Assess this cell for malaria.
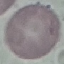
Uninfected.

preparation = thin blood smear
image type = automatically extracted cell patch, resized to 64 × 64 pixels
stain = Giemsa
capture = smartphone camera at the microscope eyepiece